Mark where platelets are.
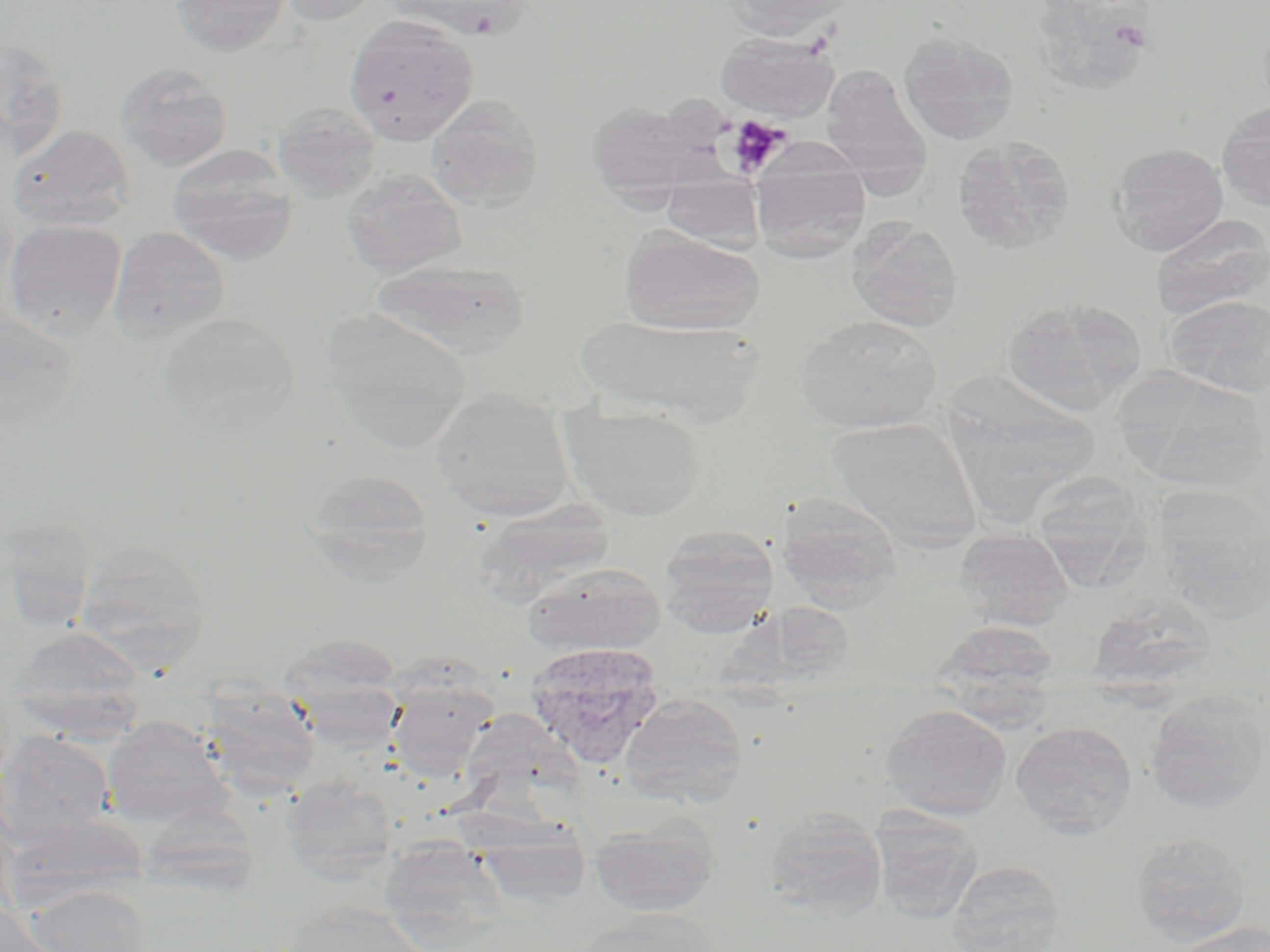

Approximate bounding boxes as [x1, y1, x2, y2] in pixels.
Platelets: [724, 116, 791, 178].

Summary:
  - Uninfected red blood cell locations: [171, 0, 290, 57], [274, 0, 383, 26], [380, 0, 534, 41], [727, 0, 858, 40], [1039, 2, 1163, 91], [345, 15, 479, 145], [898, 29, 1019, 145], [716, 33, 839, 122], [0, 34, 70, 161], [116, 61, 233, 172], [821, 65, 932, 184], [426, 93, 545, 211], [586, 99, 706, 202], [1216, 101, 1270, 212], [273, 102, 381, 203], [9, 124, 135, 231], [951, 135, 1076, 253], [1108, 142, 1229, 256], [167, 143, 298, 264], [752, 159, 870, 265], [342, 168, 467, 277], [661, 175, 765, 252], [1151, 213, 1269, 321], [4, 218, 128, 339], [848, 218, 963, 331], [108, 226, 230, 345], [621, 227, 765, 336], [371, 258, 530, 356], [1166, 295, 1270, 397], [1002, 296, 1146, 417], [0, 305, 80, 429], [323, 311, 471, 452], [158, 312, 298, 433], [795, 313, 942, 433], [573, 314, 763, 421], [1117, 367, 1267, 491], [953, 373, 1105, 517], [431, 388, 575, 523], [560, 407, 705, 519], [828, 416, 982, 550], [303, 469, 434, 583], [1037, 470, 1160, 603], [1153, 485, 1270, 619], [776, 491, 902, 611], [473, 500, 615, 608], [1, 516, 98, 632], [657, 523, 779, 637], [953, 529, 1075, 630], [76, 541, 212, 661], [522, 563, 666, 656], [1086, 593, 1216, 692], [761, 601, 857, 680], [930, 619, 1060, 701], [7, 627, 148, 739], [278, 633, 406, 740], [385, 676, 497, 780], [197, 684, 322, 799], [1145, 691, 1269, 813], [620, 692, 748, 808], [880, 704, 1012, 821], [101, 716, 236, 829], [1011, 722, 1137, 839], [0, 731, 114, 843], [283, 775, 399, 881], [764, 808, 887, 919], [871, 810, 983, 924], [2, 814, 146, 916], [589, 817, 722, 917], [470, 818, 593, 910], [1131, 831, 1251, 947], [378, 838, 505, 937], [946, 860, 1066, 952], [25, 883, 155, 952], [279, 901, 429, 952], [0, 902, 62, 951], [577, 907, 722, 952], [1170, 922, 1269, 952]
  - Plasmodium vivax-infected red blood cell locations: [524, 641, 664, 768]
  - Slide-level diagnosis: Plasmodium vivax
  - Modality: optical microscopy
  - Image size: 1270×952 pixels
  - Magnification: 1000x
  - Stain: May-Grünwald-Giemsa
  - Preparation: thin blood smear
  - Field of view: single